Name the blood parasite species.
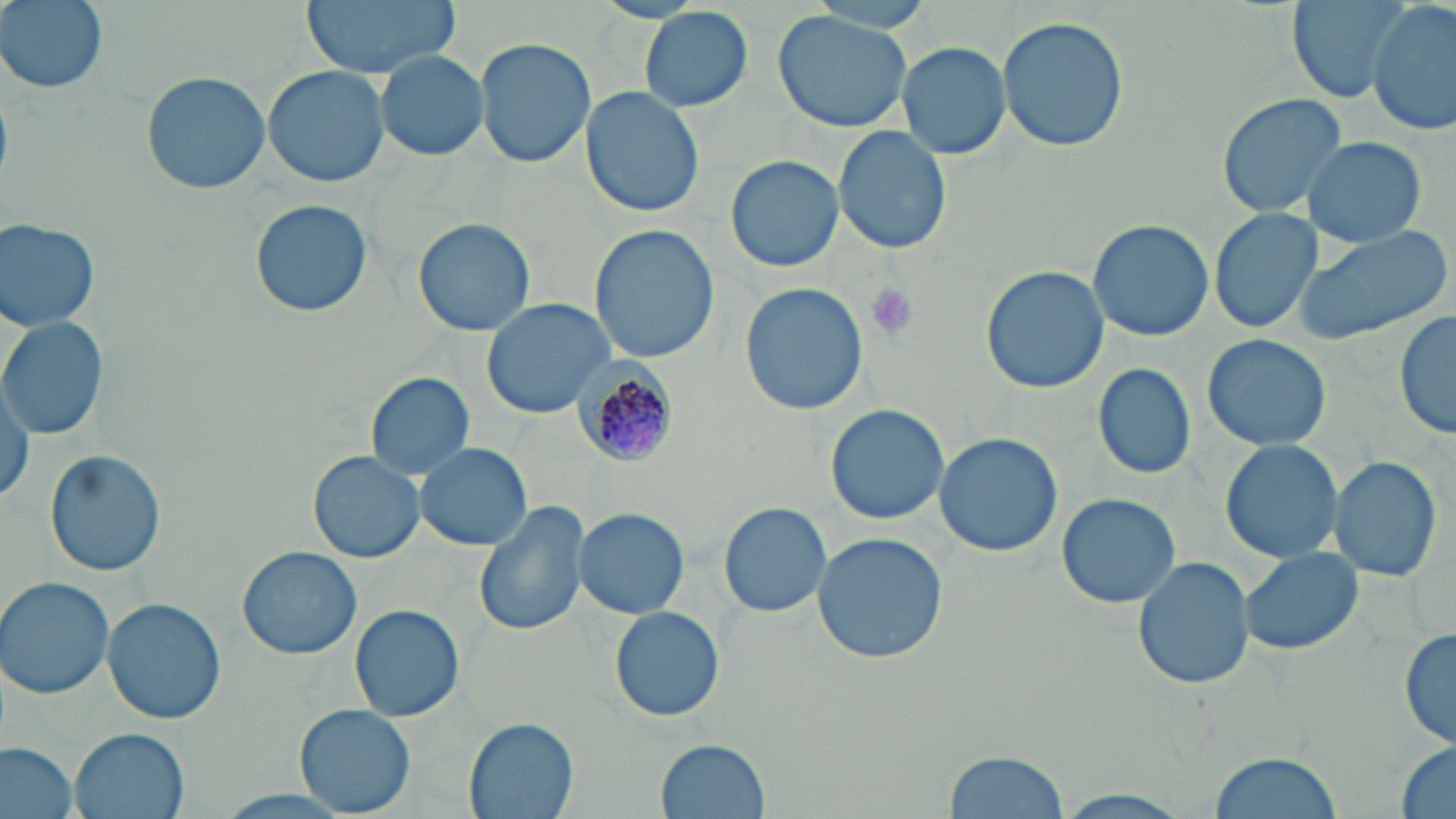

Plasmodium malariae.

stain = May-Grünwald-Giemsa
platelet locations = approximate bounding boxes as [x1, y1, x2, y2] in pixels: [861, 282, 921, 342]
preparation = thin blood film
uninfected red blood cell locations = approximate bounding boxes as [x1, y1, x2, y2] in pixels: [2, 0, 108, 94], [300, 0, 461, 79], [1284, 0, 1411, 104], [588, 1, 711, 25], [1369, 2, 1455, 137], [772, 7, 917, 133], [641, 8, 754, 111], [998, 16, 1129, 152], [475, 37, 594, 170], [897, 42, 1011, 162], [375, 50, 487, 162], [262, 64, 392, 188], [141, 70, 270, 196], [582, 87, 705, 217], [1215, 93, 1346, 217], [833, 125, 951, 254], [1302, 137, 1427, 246], [724, 154, 846, 273], [249, 198, 373, 318], [1209, 208, 1324, 333], [0, 217, 100, 331], [412, 217, 537, 337], [1087, 218, 1214, 342], [1292, 222, 1453, 346], [588, 225, 719, 365], [981, 266, 1110, 394], [738, 281, 871, 416], [481, 297, 617, 419], [1394, 309, 1456, 440], [0, 315, 108, 443], [1201, 334, 1333, 454], [1093, 362, 1197, 478], [366, 372, 474, 481], [1, 376, 34, 507], [824, 404, 950, 525], [933, 432, 1063, 558], [1220, 439, 1345, 565], [414, 441, 532, 550], [44, 449, 167, 578], [306, 449, 427, 564], [1328, 454, 1445, 583], [1056, 492, 1184, 609], [473, 499, 590, 638], [719, 502, 831, 617], [574, 509, 689, 616], [811, 533, 948, 665], [1240, 545, 1364, 657], [238, 546, 361, 659], [1133, 556, 1254, 689], [0, 576, 118, 698], [103, 598, 227, 724], [349, 605, 465, 722], [609, 607, 725, 722], [1398, 624, 1454, 754], [294, 704, 418, 817], [463, 717, 578, 819], [71, 729, 187, 818], [657, 737, 769, 817], [1393, 741, 1456, 819], [0, 743, 80, 819], [943, 749, 1069, 818], [1206, 752, 1343, 819], [1051, 789, 1196, 819], [206, 790, 364, 819]
Plasmodium malariae-infected red blood cell locations = approximate bounding boxes as [x1, y1, x2, y2] in pixels: [565, 353, 679, 471]
modality = light microscopy
image size = 1456×819 pixels
field of view = one of a larger specimen
magnification = 1000x